Classify this cell by malaria status.
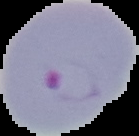

Parasitized.

image type = segmented cell region with the area outside set to black
preparation = thin blood smear
image size = 139×136 pixels